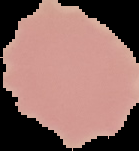
From a thin blood smear. Cell region segmented out of the field of view; the surrounding area is masked to black. Image is 139×151 pixels. Result: negative for malaria parasites.